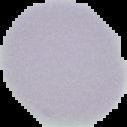

image_size: 127×127 pixels
image_type: segmented cell region on a black background
malaria_status: uninfected
preparation: thin blood smear